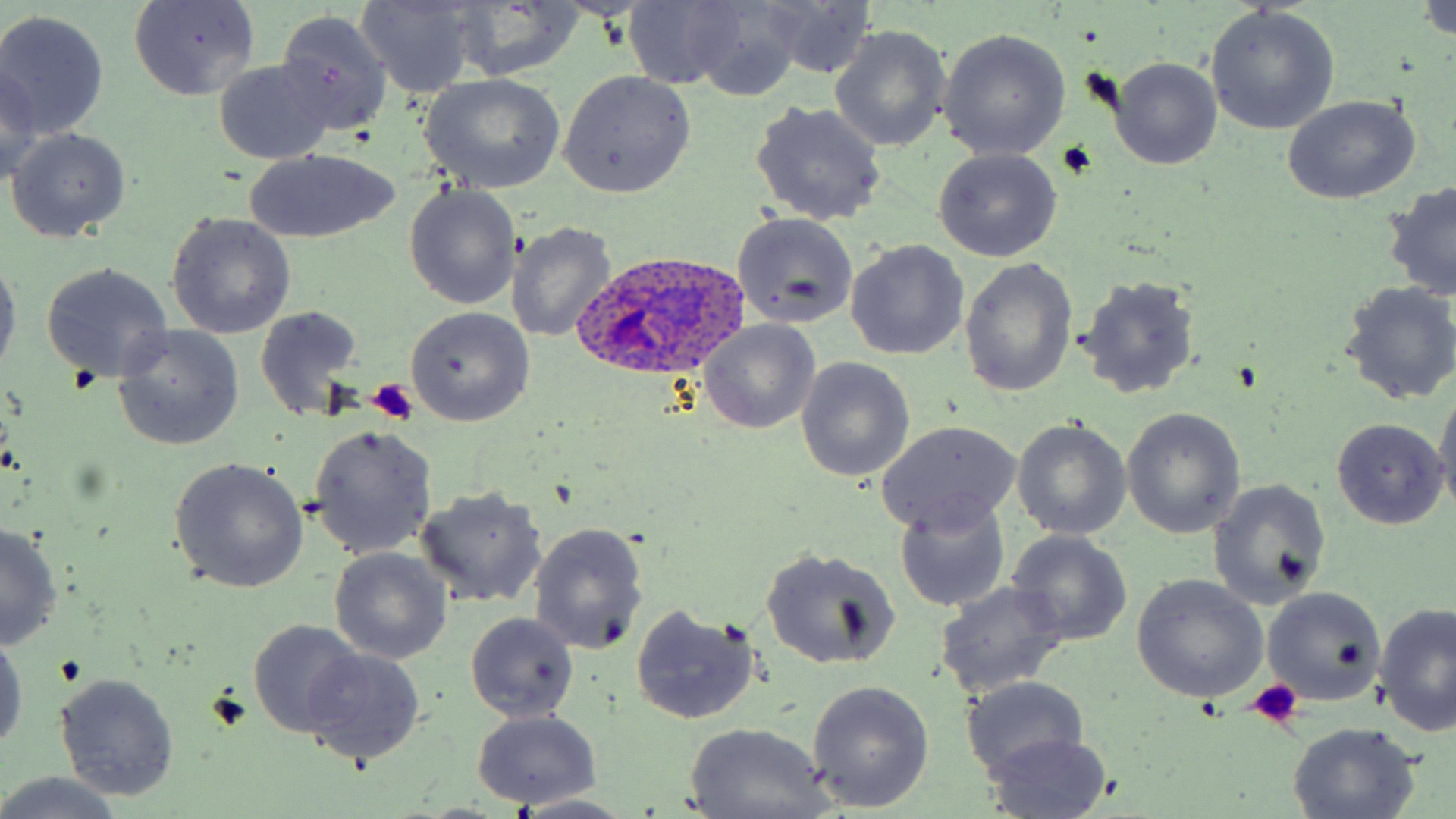
Summary:
  - Coordinate format: approximate bounding boxes as (x1, y1, x2, y2) in pixels
  - Platelet locations: (1060, 141, 1097, 180), (366, 379, 417, 424), (1248, 680, 1304, 730)
  - Plasmodium ovale-infected red blood cell locations: (573, 255, 748, 389)
  - Uninfected red blood cell locations: (355, 0, 479, 101), (684, 0, 807, 101), (752, 0, 875, 78), (1420, 0, 1456, 40), (127, 2, 262, 101), (448, 2, 584, 82), (621, 2, 741, 90), (1205, 7, 1337, 136), (0, 10, 109, 138), (276, 10, 392, 138), (830, 25, 951, 153), (939, 30, 1072, 160), (1107, 57, 1222, 169), (213, 60, 336, 163), (0, 62, 44, 186), (559, 71, 697, 197), (419, 73, 564, 193), (1281, 94, 1422, 204), (753, 103, 885, 226), (5, 128, 131, 242), (933, 148, 1063, 261), (243, 149, 401, 244), (404, 183, 522, 310), (1382, 183, 1456, 303), (732, 211, 860, 328), (165, 212, 297, 339), (507, 223, 617, 343), (845, 239, 970, 361), (0, 254, 20, 378), (960, 257, 1077, 396), (40, 263, 174, 384), (1074, 274, 1202, 399), (1338, 282, 1456, 407), (253, 305, 365, 421), (405, 307, 534, 426), (698, 319, 821, 434), (112, 325, 245, 452), (796, 357, 916, 482), (1432, 390, 1456, 515), (1122, 408, 1245, 539), (1011, 418, 1132, 540), (874, 419, 1022, 534), (1331, 419, 1446, 529), (307, 423, 438, 560), (171, 457, 308, 594), (1207, 479, 1329, 610), (414, 487, 548, 608), (894, 498, 1011, 612), (528, 522, 648, 656), (0, 523, 64, 649), (1006, 530, 1133, 646), (331, 547, 452, 664), (760, 547, 901, 670), (1132, 575, 1269, 704), (936, 582, 1069, 699), (1261, 586, 1386, 706), (1374, 603, 1455, 737), (629, 604, 762, 724), (465, 613, 580, 722), (247, 619, 366, 738), (0, 627, 26, 751), (302, 649, 423, 766), (54, 672, 180, 801), (959, 675, 1090, 781), (806, 680, 934, 812), (470, 711, 601, 808), (1287, 721, 1423, 818), (683, 722, 833, 819), (982, 731, 1112, 817), (0, 771, 129, 819), (512, 794, 635, 818)
  - Slide-level diagnosis: Plasmodium ovale
  - Stain: May-Grünwald-Giemsa
  - Preparation: thin blood smear
  - Image size: 1456×819 pixels
  - Magnification: 1000x
  - Modality: light microscopy
  - Field of view: one of a larger specimen